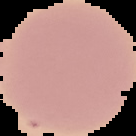

Summary:
  - Result: no Plasmodium parasites seen
  - Image size: 136×136 pixels
  - Preparation: thin blood film
  - Image type: cell region segmented out of the field of view; surrounding area masked to black